Give the position of every Plasmodium parasite visible.
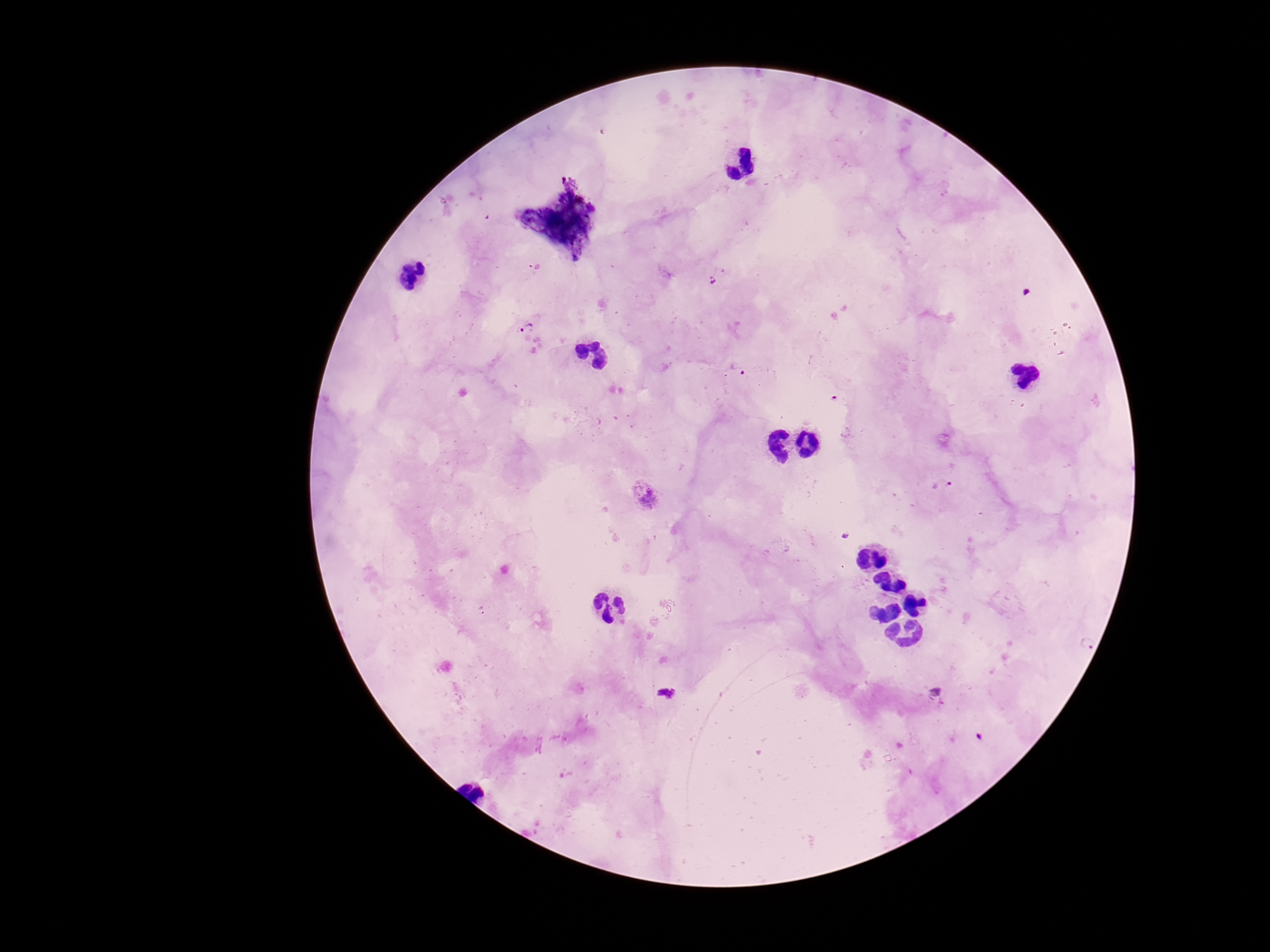

Approximate centers as {x, y} in pixels.
Plasmodium parasites: {711, 279}, {526, 329}, {740, 368}, {941, 484}, {648, 498}.

Image is 1270×952 pixels. Photographed through the microscope eyepiece with a smartphone camera. Thick blood smear. One field from this slide. Patient malaria status: infected. Giemsa stain. 100x magnification.